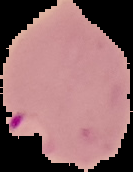
image type = segmented cell region with the area outside set to black
preparation = thin blood film
image size = 133×172 pixels
result = Plasmodium parasites detected